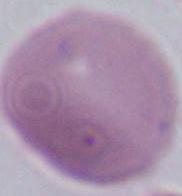

Photomicrograph. 1000x magnification. An erythrocyte is shown.